Comment on the morphology of the erythrocytes.
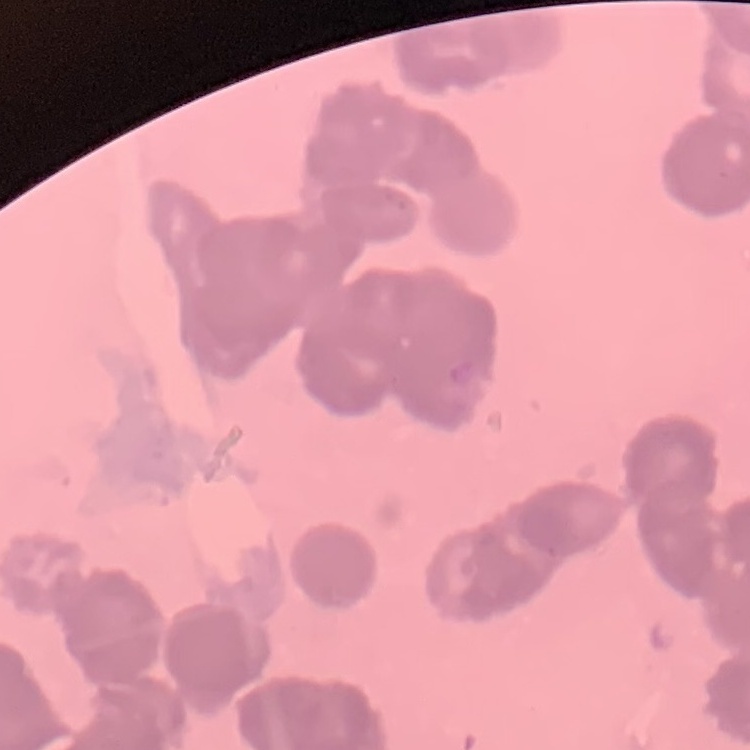

They show rouleaux formation.

Square crop of a larger photomicrograph. Stained with either Field's or Giemsa. Thin blood film.